Comment on the morphology of the erythrocytes.
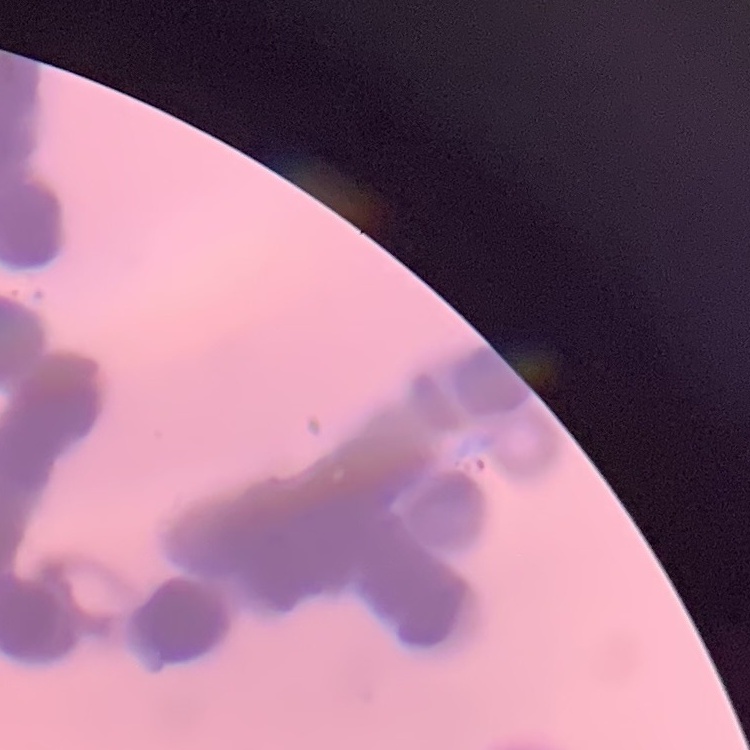

They show rouleaux formation.

Thin blood smear. One tile cut from a larger photomicrograph. Field's or Giemsa stain.